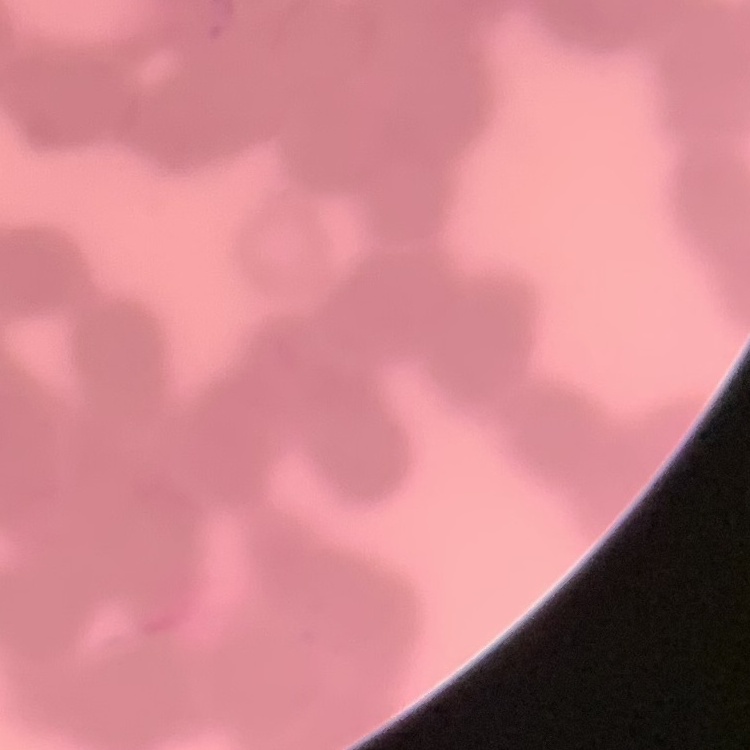
{
  "red_blood_cell_morphology": "rouleaux formation",
  "preparation": "thin blood film",
  "stain": "Field's or Giemsa",
  "image_type": "one tile cut from a larger photomicrograph"
}